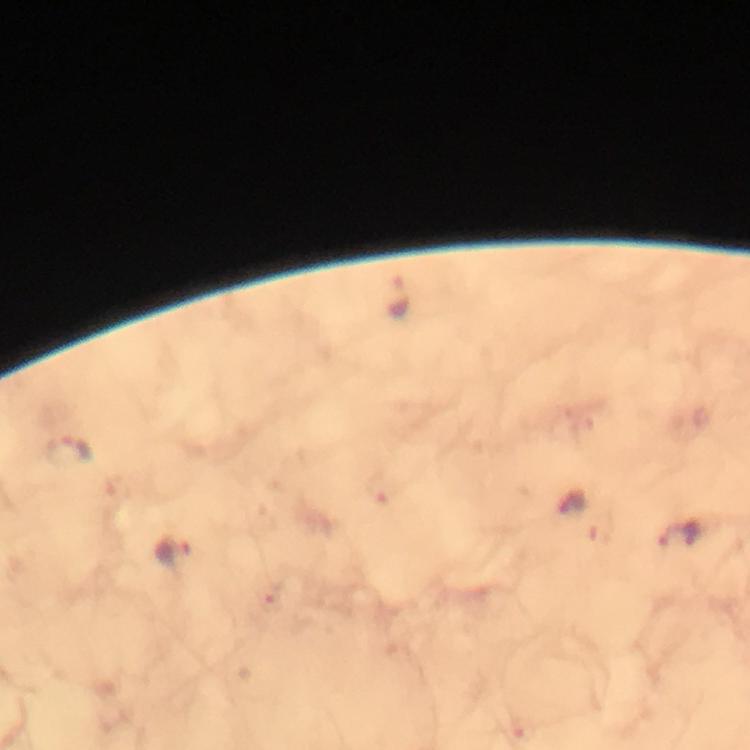
Approximate object centers, in pixels from the top-left corner. Plasmodium parasite locations: (x=398, y=298), (x=71, y=453), (x=573, y=503), (x=682, y=533), (x=175, y=551). Thick blood film. At 100x magnification. Immersion oil was used. Cropped region of a single field of view. Giemsa stain. Photographed through the microscope with a smartphone camera. From a malaria diagnostic workup. Image is 750×750 pixels.